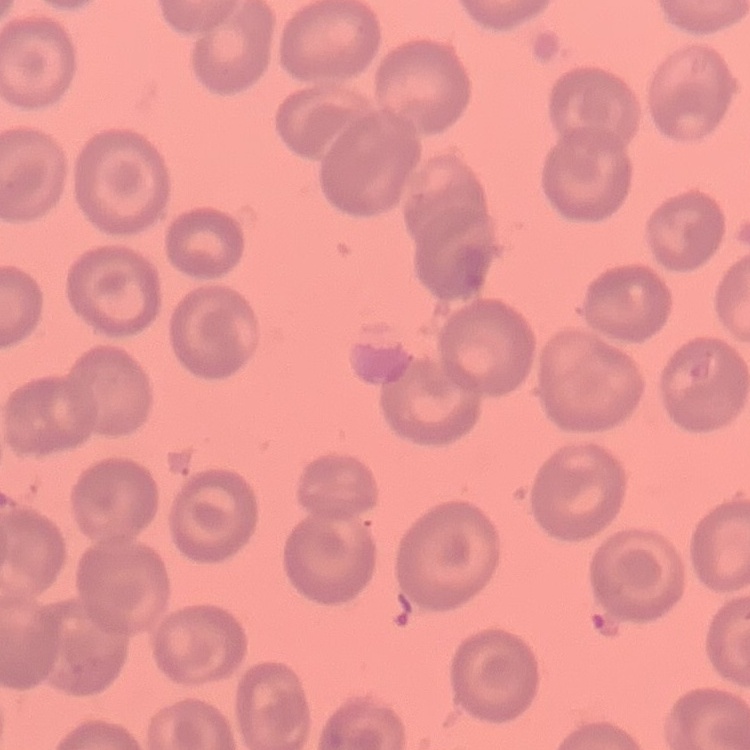

The erythrocytes show no rouleaux formation. Thin blood smear. Stained with either Field's or Giemsa. One tile cut from a larger photomicrograph.